Identify the preparation type.
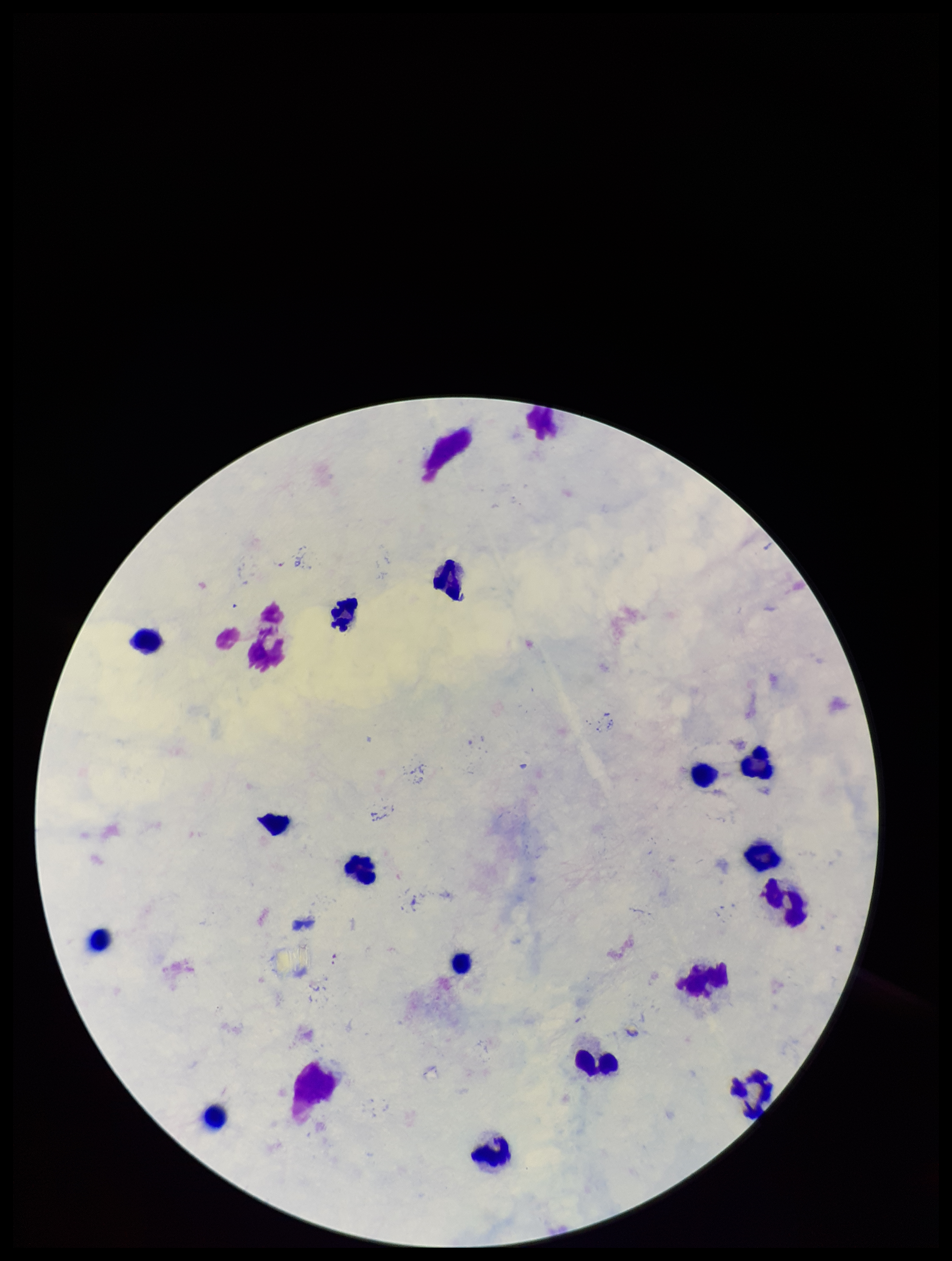

It is a thick blood smear.

Summary:
  - Image size: 952×1261 pixels
  - Patient malaria status: infected
  - Field of view: single
  - Parasite count: 0
  - Species reported for this patient: Plasmodium falciparum
  - Leukocyte count: 16
  - Capture: smartphone photograph through the microscope eyepiece
  - Stain: Giemsa
  - Plasmodium parasites: none seen